State which parasite is depicted.
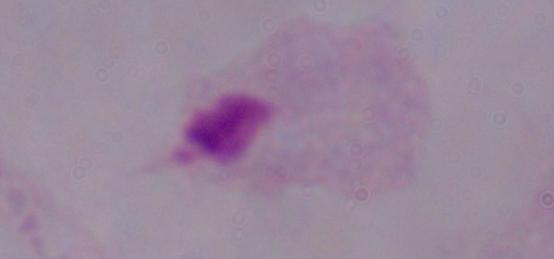

This is a trichomonad.

Micrograph. Captured at 1000x magnification.